Assess this cell for malaria.
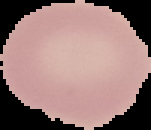
It is uninfected.

Image is 151×130 pixels. Segmented cell region on a black background. From a thin blood smear.